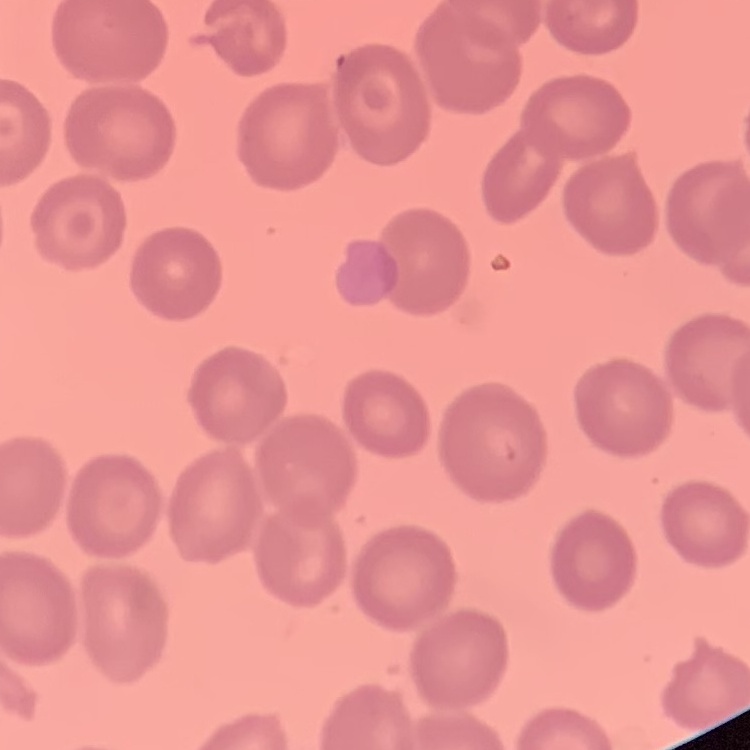
The red blood cells show no rouleaux formation. Stained with either Field's or Giemsa. Square crop of a larger photomicrograph. Thin blood film.